Comment on the morphology of the red blood cells.
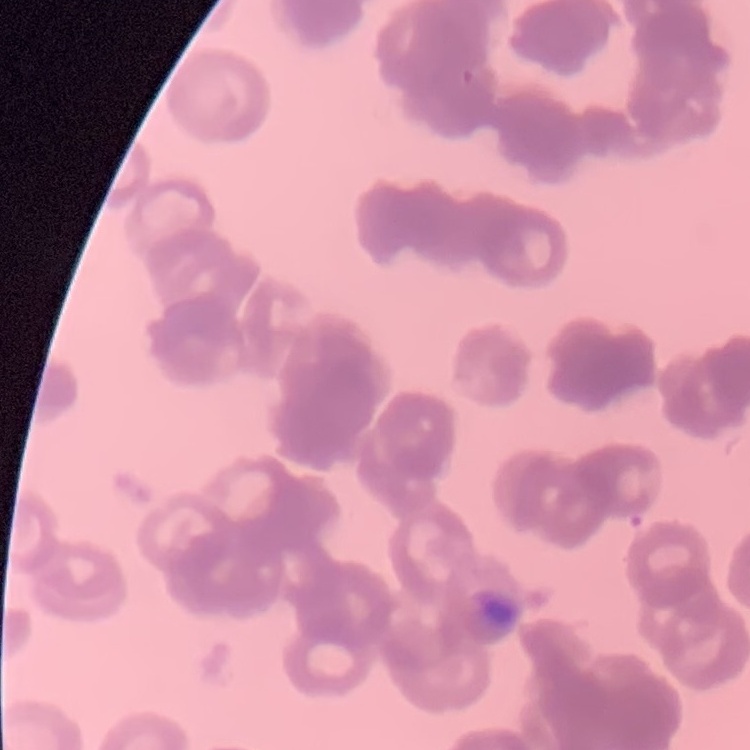

Rouleaux formation.

Field's or Giemsa stain. Square crop of a larger photomicrograph. Thin blood smear.